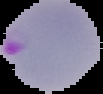

Result: malaria parasites identified. Segmented cell region on a black background. From a thin blood smear. Image is 103×94 pixels.